Classify this cell by malaria status.
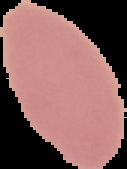
It is uninfected.

image size = 127×169 pixels
preparation = thin blood film
image type = segmented cell region with the area outside set to black